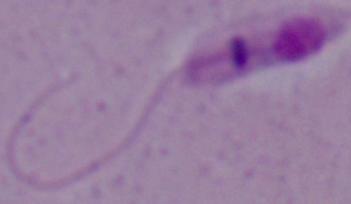

modality = micrograph
magnification = 1000x
identification = Leishmania